Outline each uninfected red blood cell.
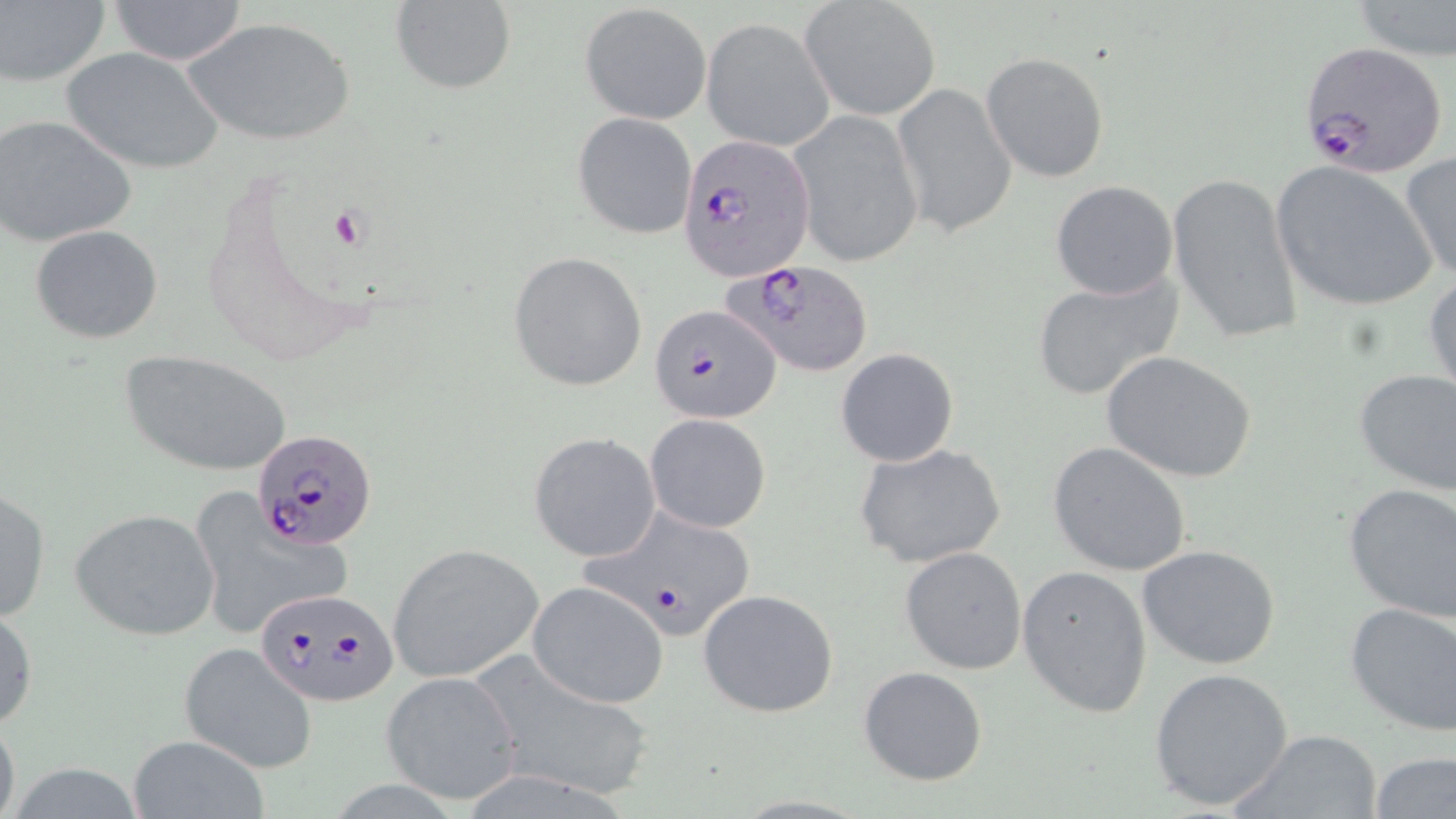
Approximate bounding boxes as (x1,y1)-(x2,y2) corner pairs in pixels.
Uninfected red blood cells: (104,0)-(250,65), (1,1)-(111,88), (800,1)-(942,121), (1350,1)-(1456,60), (389,2)-(517,94), (579,3)-(712,126), (183,17)-(358,148), (702,17)-(834,149), (61,46)-(227,174), (980,52)-(1110,182), (890,83)-(1017,239), (788,109)-(925,271), (571,113)-(698,239), (1,116)-(138,246), (1399,153)-(1455,284), (1271,161)-(1438,313), (1167,173)-(1303,344), (1050,180)-(1179,301), (30,224)-(164,344), (509,252)-(648,392), (1424,269)-(1456,403), (1028,271)-(1183,401), (119,348)-(295,477), (835,348)-(960,467), (1101,350)-(1257,485), (1352,369)-(1456,496), (646,414)-(770,533), (528,432)-(661,562), (1048,442)-(1191,576), (856,444)-(1007,571), (1342,484)-(1456,624), (1,485)-(51,624), (184,493)-(352,643), (70,508)-(221,641), (386,543)-(545,683), (1137,544)-(1282,668), (900,547)-(1027,675), (1017,565)-(1154,718), (527,582)-(669,708), (697,588)-(841,719), (1344,599)-(1456,735), (0,601)-(37,732), (177,643)-(318,774), (469,653)-(654,800), (858,666)-(988,786), (1148,666)-(1295,812), (380,671)-(524,805), (0,711)-(21,819), (1227,728)-(1385,817), (129,737)-(266,816), (1371,753)-(1456,819).

Plasmodium falciparum-infected red blood cell locations: (1297,41)-(1449,178), (677,134)-(812,280), (723,258)-(875,377), (649,302)-(780,424), (251,429)-(379,551), (579,505)-(759,644), (254,587)-(398,708). Platelet locations: (328,205)-(369,249). Slide-level diagnosis: Plasmodium falciparum. Single field of view. Image is 1456×819 pixels. May-Grünwald-Giemsa stain. 1000x magnification. Thin blood film. Light microscopy.